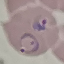
result: malaria parasites identified
preparation: thin blood smear
capture: smartphone camera at the microscope eyepiece
image_type: cell patch, automatically extracted from a larger field of view and resized to 64 × 64 pixels
stain: Giemsa